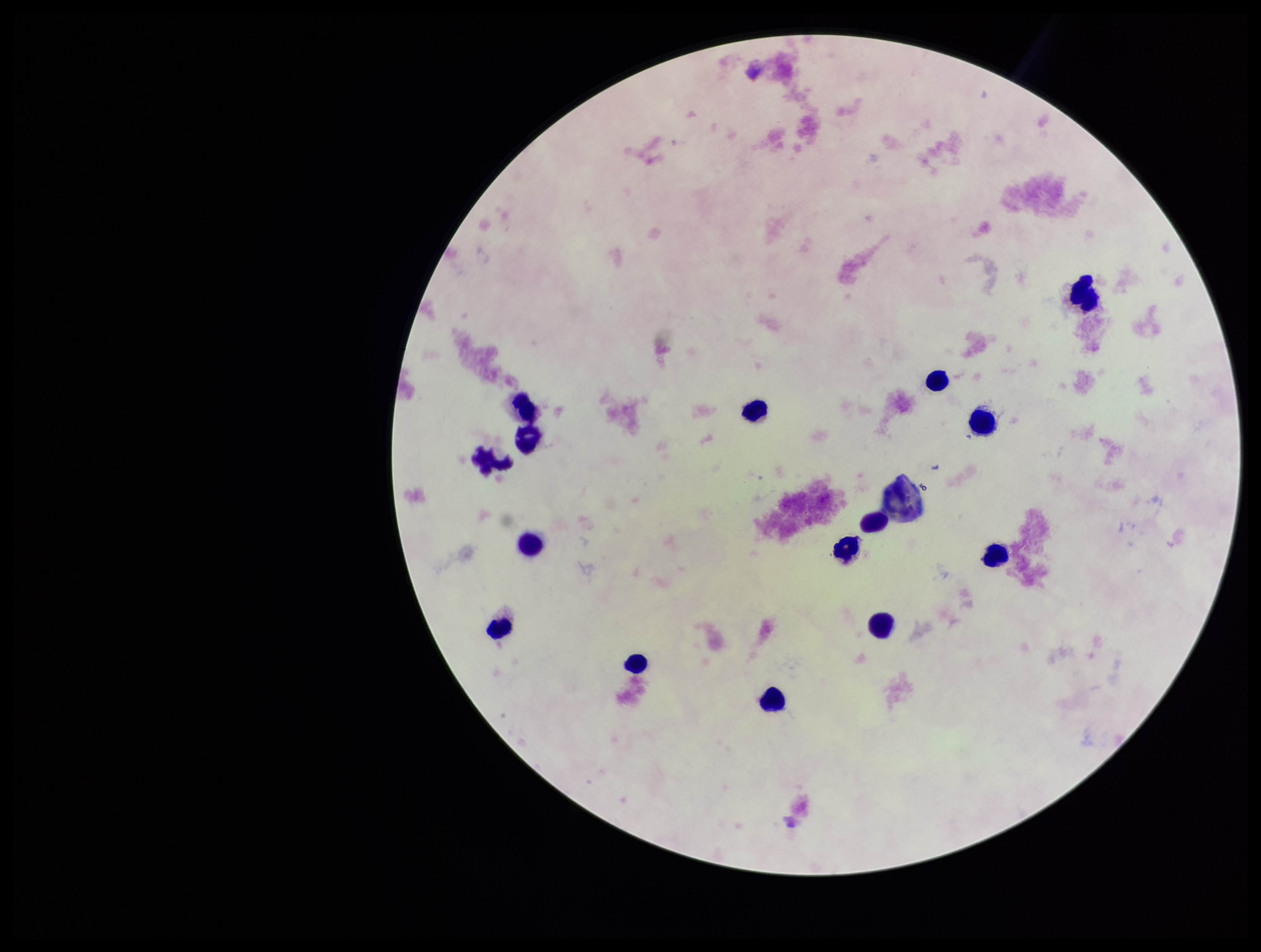

Patient malaria status: negative. Plasmodium parasites: none detected. Preparation: thick smear. Parasite count: 0. One field from this slide. Leukocyte count: 15. Image is 1261×952 pixels. Stained with Giemsa. Photographed through the microscope eyepiece with a smartphone camera.